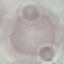

Result: no malaria parasites seen. Giemsa-stained preparation. Photographed with a smartphone camera at the microscope eyepiece. Thin blood smear. Automatically extracted cell patch, resized to 64 × 64 pixels.